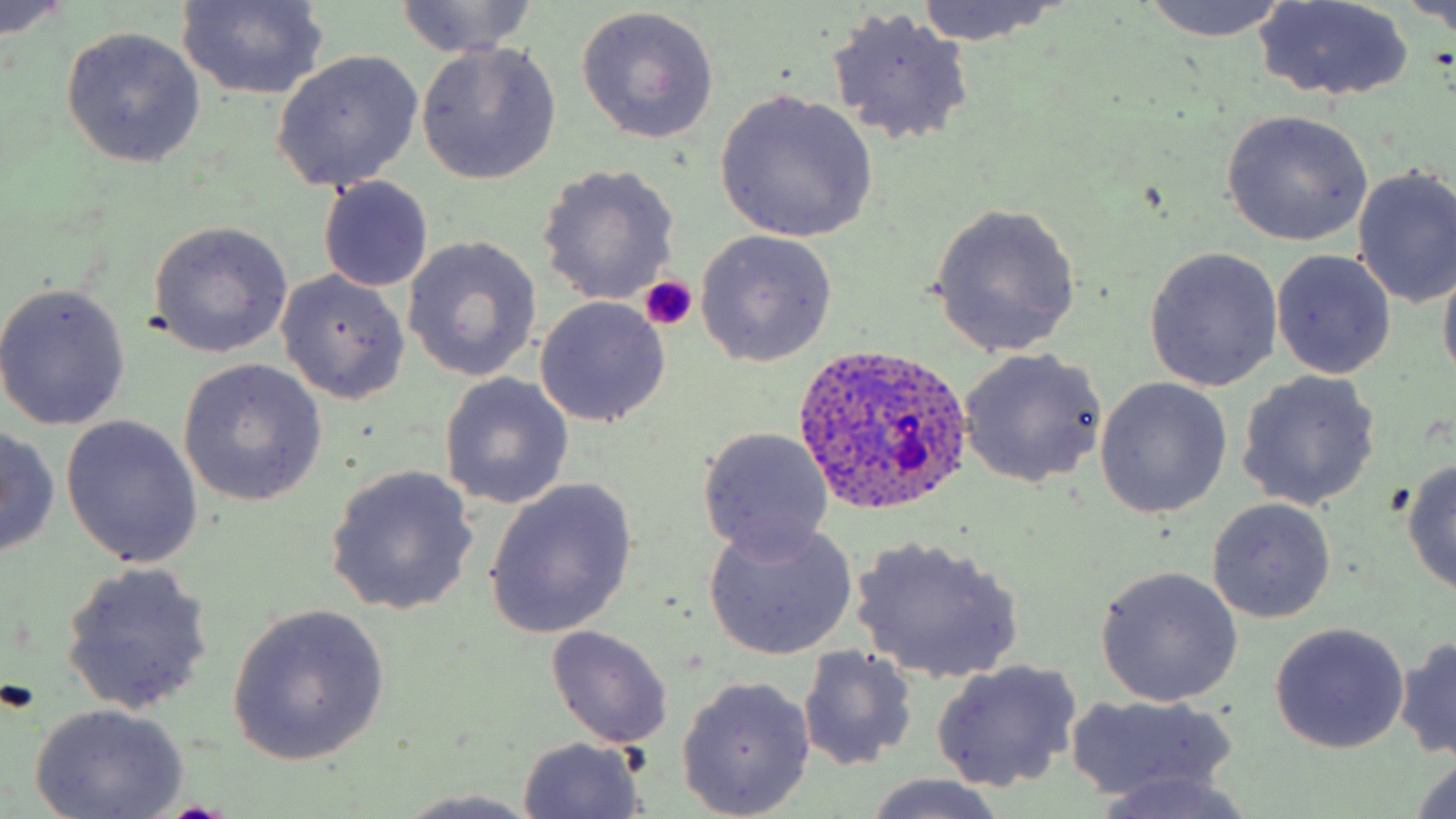

{
  "slide_level_diagnosis": "Plasmodium ovale",
  "preparation": "thin blood film",
  "stain": "May-Grünwald-Giemsa",
  "field_of_view": "one of a larger specimen",
  "plasmodium_ovale_infected_red_blood_cell_locations": "approximate bounding boxes as (x1,y1)-(x2,y2) corner pairs in pixels: (788,343)-(976,520)",
  "modality": "optical microscopy",
  "image_size": "1456×819 pixels",
  "magnification": "1000x",
  "uninfected_red_blood_cell_locations": "approximate bounding boxes as (x1,y1)-(x2,y2) corner pairs in pixels: (393,0)-(540,58), (913,0)-(1062,47), (1135,0)-(1292,42), (1254,0)-(1413,103), (1407,0)-(1456,35), (176,1)-(330,102), (0,3)-(73,38), (575,5)-(721,144), (826,8)-(976,148), (60,26)-(206,168), (415,43)-(561,184), (271,50)-(425,192), (713,89)-(878,242), (1219,111)-(1374,247), (536,164)-(682,307), (1351,168)-(1456,308), (318,177)-(434,292), (927,203)-(1083,355), (147,221)-(294,358), (693,230)-(838,366), (402,236)-(543,383), (1143,248)-(1283,392), (1271,250)-(1396,379), (1438,251)-(1456,388), (277,270)-(409,403), (0,281)-(132,432), (535,296)-(671,426), (957,348)-(1107,489), (177,360)-(328,507), (1235,370)-(1382,512), (438,372)-(574,510), (1095,378)-(1230,517), (60,415)-(205,567), (1,422)-(61,555), (696,426)-(836,560), (1401,458)-(1456,596), (325,465)-(480,616), (484,479)-(638,639), (1207,498)-(1335,624), (702,518)-(858,661), (852,535)-(1025,683), (59,561)-(215,714), (1096,566)-(1244,708), (227,605)-(390,766), (1269,623)-(1409,754), (545,626)-(673,751), (1395,634)-(1456,762), (797,647)-(917,772), (931,660)-(1080,792), (677,676)-(817,817), (1066,695)-(1240,804), (28,703)-(190,819), (516,737)-(649,818), (1411,753)-(1456,817), (1091,773)-(1262,819), (858,776)-(1017,819), (390,790)-(545,818)",
  "platelet_locations": "approximate bounding boxes as (x1,y1)-(x2,y2) corner pairs in pixels: (637,276)-(696,331)"
}